Report the malaria status of this cell.
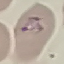
Parasitized.

Summary:
  - Image type: automatically extracted cell patch, resized to 64 × 64 pixels
  - Preparation: thin blood smear
  - Stain: Giemsa
  - Capture: smartphone camera at the microscope eyepiece